Outline each blood parasite and name the species.
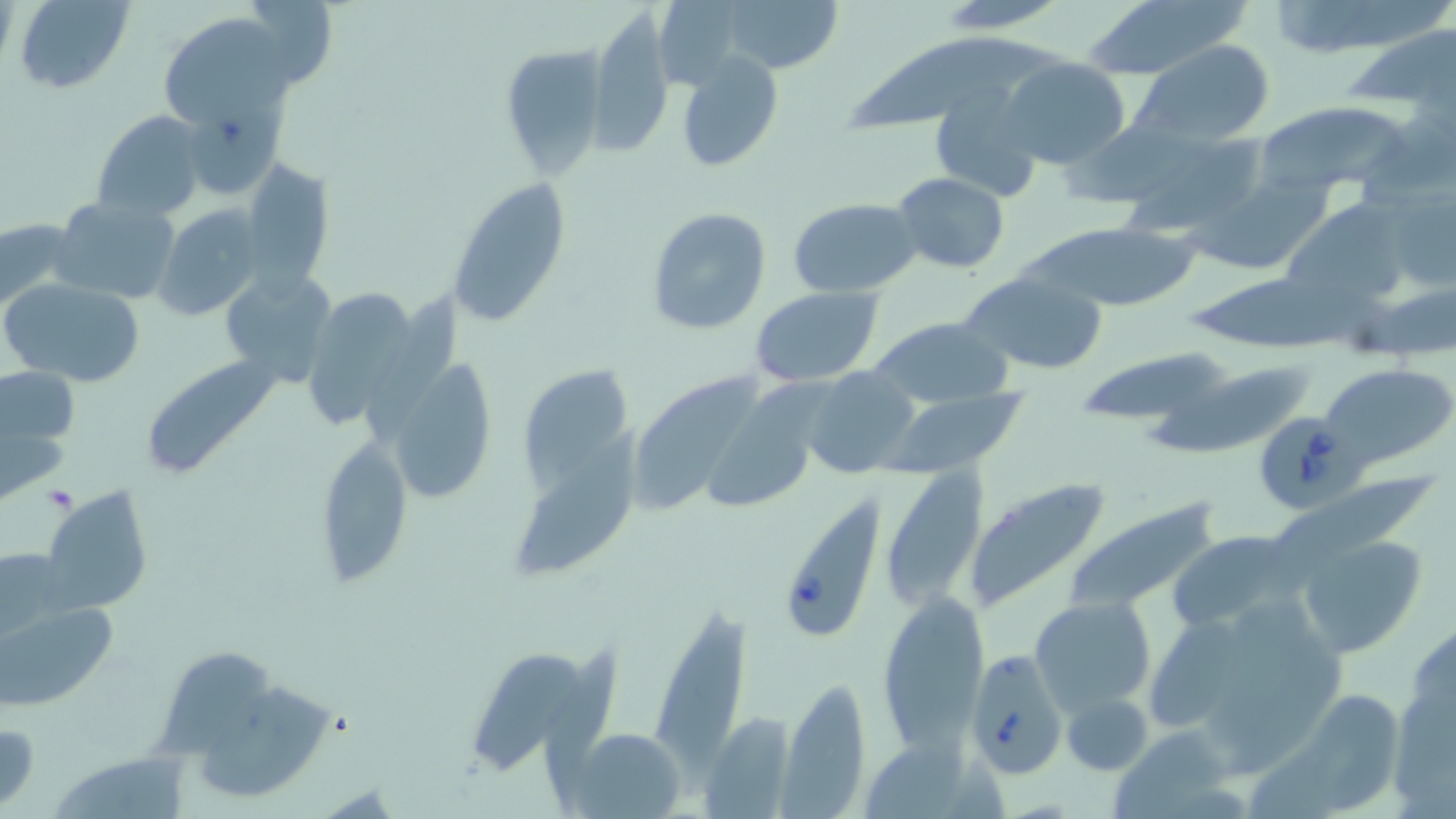

Approximate bounding boxes as named x1/y1/x2/y2 corners in pixels.
Babesia divergens-infected red blood cells: (x1=1256, y1=412, x2=1356, y2=510), (x1=774, y1=492, x2=888, y2=642), (x1=966, y1=649, x2=1068, y2=776).
No Plasmodium falciparum, Plasmodium ovale, Plasmodium malariae, Plasmodium vivax, or Trypanosoma brucei observed.

Summary:
  - Uninfected red blood cell locations: (x1=12, y1=0, x2=134, y2=94), (x1=254, y1=0, x2=335, y2=85), (x1=716, y1=0, x2=844, y2=77), (x1=933, y1=0, x2=1070, y2=30), (x1=1081, y1=0, x2=1253, y2=80), (x1=1273, y1=0, x2=1454, y2=49), (x1=655, y1=2, x2=743, y2=92), (x1=589, y1=7, x2=676, y2=160), (x1=154, y1=16, x2=296, y2=127), (x1=1339, y1=19, x2=1456, y2=116), (x1=851, y1=37, x2=1066, y2=137), (x1=1133, y1=39, x2=1276, y2=147), (x1=500, y1=45, x2=609, y2=179), (x1=676, y1=52, x2=784, y2=172), (x1=999, y1=56, x2=1132, y2=171), (x1=182, y1=79, x2=288, y2=199), (x1=932, y1=85, x2=1044, y2=199), (x1=1254, y1=101, x2=1413, y2=193), (x1=93, y1=110, x2=207, y2=222), (x1=1054, y1=114, x2=1226, y2=202), (x1=1360, y1=118, x2=1456, y2=210), (x1=1118, y1=133, x2=1270, y2=237), (x1=240, y1=158, x2=331, y2=294), (x1=891, y1=172, x2=1011, y2=274), (x1=1185, y1=172, x2=1342, y2=275), (x1=447, y1=180, x2=571, y2=326), (x1=1393, y1=192, x2=1456, y2=289), (x1=773, y1=195, x2=908, y2=386), (x1=53, y1=196, x2=181, y2=305), (x1=789, y1=197, x2=921, y2=298), (x1=1283, y1=198, x2=1416, y2=309), (x1=154, y1=204, x2=266, y2=322), (x1=646, y1=206, x2=772, y2=336), (x1=0, y1=217, x2=81, y2=318), (x1=1023, y1=222, x2=1199, y2=314), (x1=219, y1=268, x2=337, y2=387), (x1=1189, y1=270, x2=1398, y2=347), (x1=961, y1=272, x2=1108, y2=375), (x1=4, y1=277, x2=146, y2=387), (x1=309, y1=280, x2=419, y2=424), (x1=749, y1=287, x2=885, y2=386), (x1=368, y1=289, x2=466, y2=435), (x1=1357, y1=289, x2=1456, y2=355), (x1=864, y1=317, x2=1013, y2=410), (x1=1082, y1=345, x2=1232, y2=422), (x1=389, y1=353, x2=497, y2=506), (x1=138, y1=354, x2=281, y2=481), (x1=518, y1=362, x2=643, y2=494), (x1=1142, y1=362, x2=1314, y2=455), (x1=1325, y1=363, x2=1455, y2=465), (x1=0, y1=367, x2=78, y2=443), (x1=803, y1=367, x2=917, y2=478), (x1=632, y1=368, x2=764, y2=511), (x1=709, y1=378, x2=821, y2=512), (x1=886, y1=389, x2=1032, y2=476), (x1=517, y1=429, x2=653, y2=574), (x1=315, y1=431, x2=413, y2=585), (x1=879, y1=469, x2=989, y2=609), (x1=1271, y1=477, x2=1444, y2=564), (x1=963, y1=478, x2=1111, y2=613), (x1=43, y1=486, x2=153, y2=613), (x1=1063, y1=497, x2=1226, y2=615), (x1=1166, y1=530, x2=1301, y2=635), (x1=1297, y1=532, x2=1429, y2=657), (x1=0, y1=547, x2=62, y2=634), (x1=0, y1=591, x2=119, y2=714), (x1=877, y1=594, x2=988, y2=750), (x1=1205, y1=597, x2=1317, y2=736), (x1=1030, y1=598, x2=1156, y2=715), (x1=1152, y1=610, x2=1246, y2=732), (x1=650, y1=615, x2=754, y2=793), (x1=1403, y1=623, x2=1456, y2=733), (x1=470, y1=635, x2=590, y2=774), (x1=541, y1=645, x2=623, y2=794), (x1=1224, y1=646, x2=1353, y2=774), (x1=154, y1=651, x2=278, y2=754), (x1=781, y1=678, x2=872, y2=814), (x1=197, y1=684, x2=338, y2=801), (x1=1387, y1=688, x2=1456, y2=814), (x1=1063, y1=692, x2=1152, y2=775), (x1=1310, y1=692, x2=1403, y2=816), (x1=705, y1=710, x2=792, y2=817), (x1=0, y1=719, x2=41, y2=811), (x1=1104, y1=725, x2=1246, y2=819), (x1=860, y1=727, x2=969, y2=819), (x1=561, y1=731, x2=685, y2=815), (x1=1244, y1=743, x2=1339, y2=819), (x1=51, y1=750, x2=192, y2=819)
  - Platelet locations: (x1=42, y1=483, x2=78, y2=513)
  - Slide-level diagnosis: Babesia divergens
  - Magnification: 1000x
  - Stain: May-Grünwald-Giemsa
  - Preparation: thin blood film
  - Field of view: single
  - Modality: optical microscopy
  - Image size: 1456×819 pixels